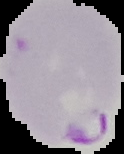
Summary:
  - Image size: 124×154 pixels
  - Preparation: thin blood smear
  - Image type: cell region segmented out of the field of view; surrounding area masked to black
  - Result: Plasmodium parasites identified